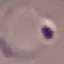
result = malaria parasites identified
image type = cell patch, automatically extracted from a larger field of view and resized to 64 × 64 pixels
capture = smartphone camera at the microscope eyepiece
preparation = thin smear
stain = Giemsa